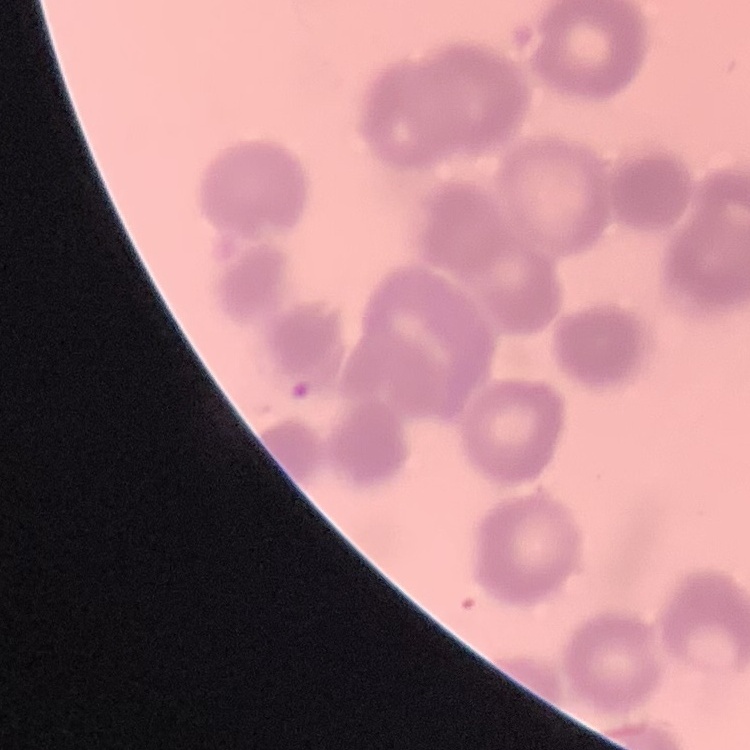
red_blood_cell_morphology: rouleaux formation
image_type: one tile cut from a larger photomicrograph
stain: Field's or Giemsa
preparation: thin blood smear